State which parasite is depicted.
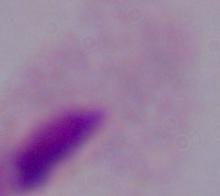

A trichomonad.

Photomicrograph. Captured at 1000x magnification.